Report the malaria status of this cell.
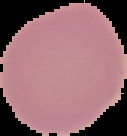
It is uninfected.

Summary:
  - Image size: 127×136 pixels
  - Preparation: thin blood smear
  - Image type: cell region segmented out of the field of view; surrounding area masked to black